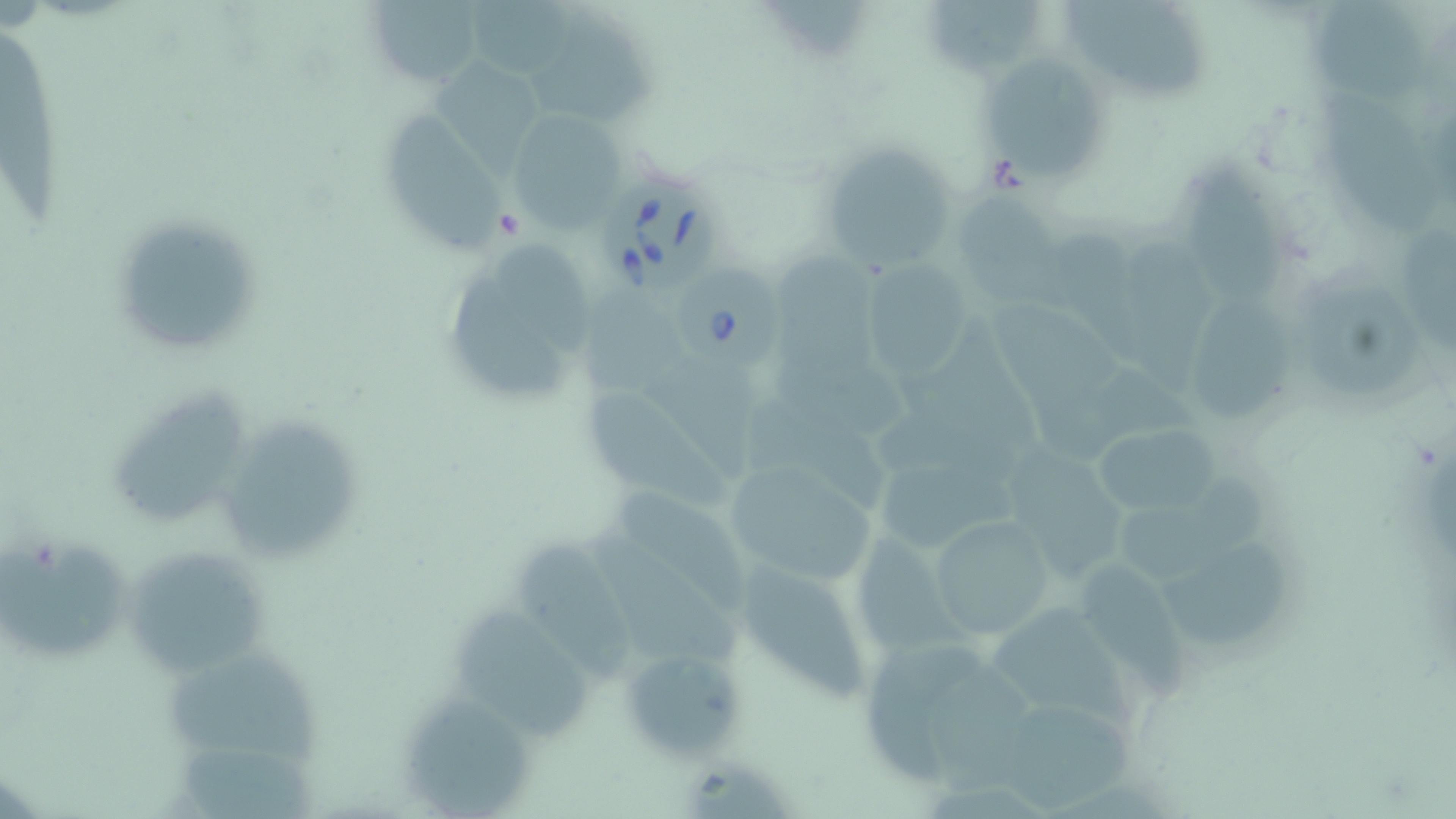
Summary:
  - Coordinate format: approximate bounding boxes as [x1, y1, x2, y2] in pixels
  - Uninfected red blood cell locations: [366, 0, 484, 87], [467, 0, 576, 78], [923, 0, 1047, 78], [1064, 0, 1205, 100], [1308, 1, 1424, 107], [524, 20, 652, 128], [1, 34, 64, 233], [426, 56, 541, 176], [984, 60, 1103, 182], [1320, 89, 1436, 231], [386, 107, 504, 256], [504, 107, 626, 231], [814, 134, 967, 273], [1179, 168, 1289, 309], [952, 185, 1079, 317], [107, 211, 269, 358], [1397, 221, 1456, 357], [1119, 233, 1215, 394], [492, 240, 594, 357], [780, 253, 882, 374], [861, 256, 977, 383], [449, 275, 568, 396], [1299, 275, 1426, 395], [582, 291, 701, 409], [1191, 292, 1295, 424], [993, 296, 1133, 425], [899, 321, 1047, 462], [592, 387, 738, 507], [115, 388, 247, 521], [743, 390, 884, 509], [227, 422, 359, 563], [1076, 422, 1225, 520], [1016, 449, 1129, 585], [718, 456, 880, 589], [877, 461, 1025, 547], [1120, 471, 1263, 571], [617, 491, 760, 614], [931, 516, 1058, 637], [594, 525, 739, 671], [4, 531, 135, 660], [855, 532, 965, 653], [128, 542, 268, 676], [522, 544, 637, 686], [1167, 549, 1289, 654], [739, 558, 871, 702], [1073, 559, 1189, 707], [992, 601, 1144, 731], [452, 604, 591, 746], [867, 629, 992, 785], [619, 644, 747, 765], [165, 654, 317, 769], [925, 659, 1049, 803], [403, 690, 533, 815], [1000, 705, 1139, 809], [180, 749, 316, 819]
  - Babesia divergens-infected red blood cell locations: [609, 180, 720, 294], [674, 260, 784, 371]
  - Slide-level diagnosis: Babesia divergens
  - Modality: light microscopy
  - Image size: 1456×819 pixels
  - Preparation: thin blood film
  - Magnification: 1000x
  - Field of view: one of a larger specimen
  - Stain: May-Grünwald-Giemsa